Give the position of each P. falciparum parasite with its life-cycle stage, each leukocyte, and any debris.
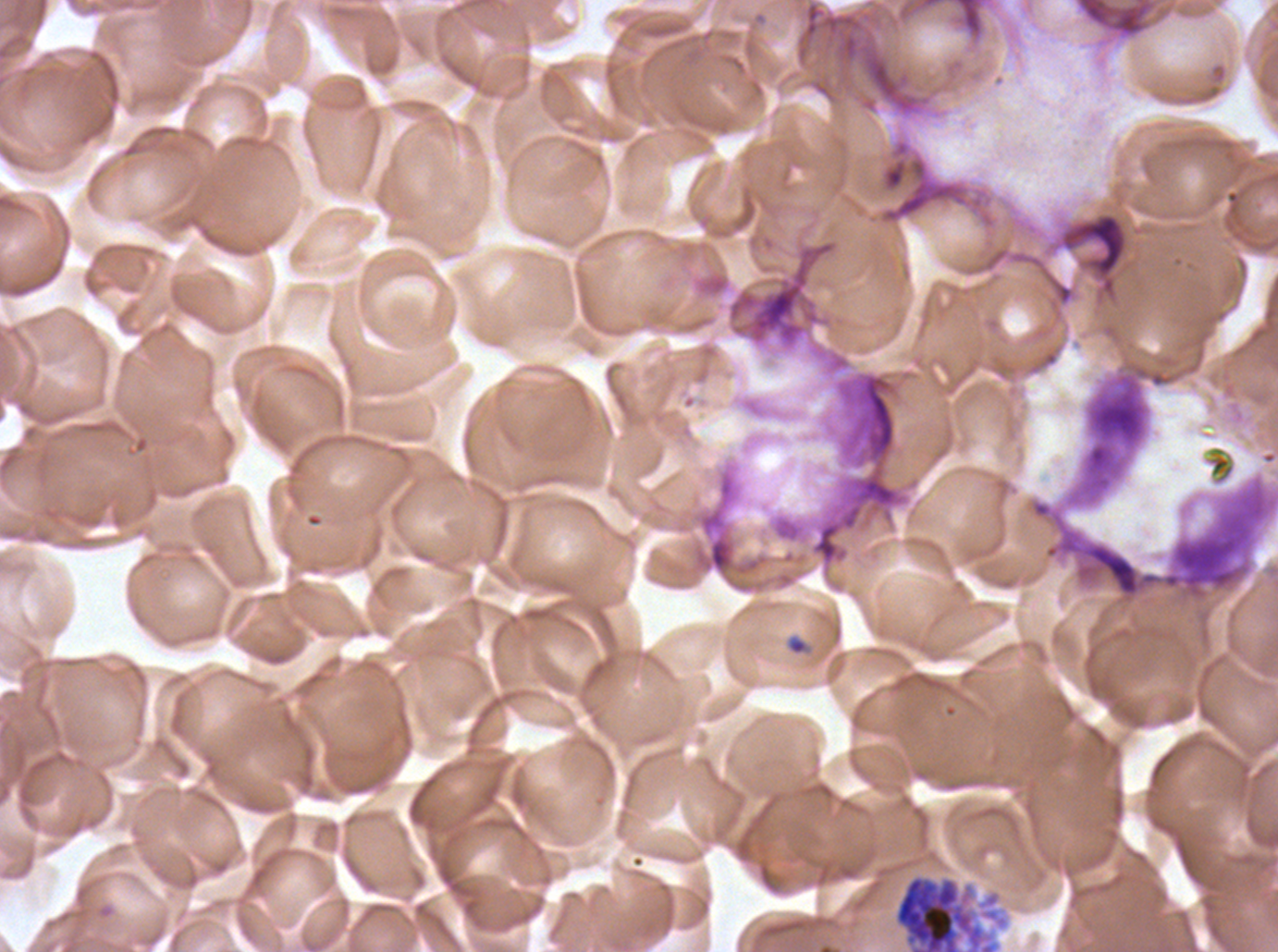

Approximate bounding boxes as [x1, y1, x2, y2] in pixels.
Segmenters: [891, 871, 1011, 951].
Debris: [867, 135, 998, 231], [1064, 364, 1175, 508], [809, 370, 911, 571], [785, 634, 809, 656].
No rings, late-ring/early-trophozoite forms, mid trophozoites, late trophozoites, early schizonts, late schizonts, gametocytes, or leukocytes observed.

Summary:
  - Field of view: one sub-image of a larger composite
  - Preparation: thin blood film
  - Stain: Giemsa
  - Image size: 1278×952 pixels
  - Specimen: ex-vivo P. falciparum culture from a patient in The Gambia, grown for 24 to 48 hours